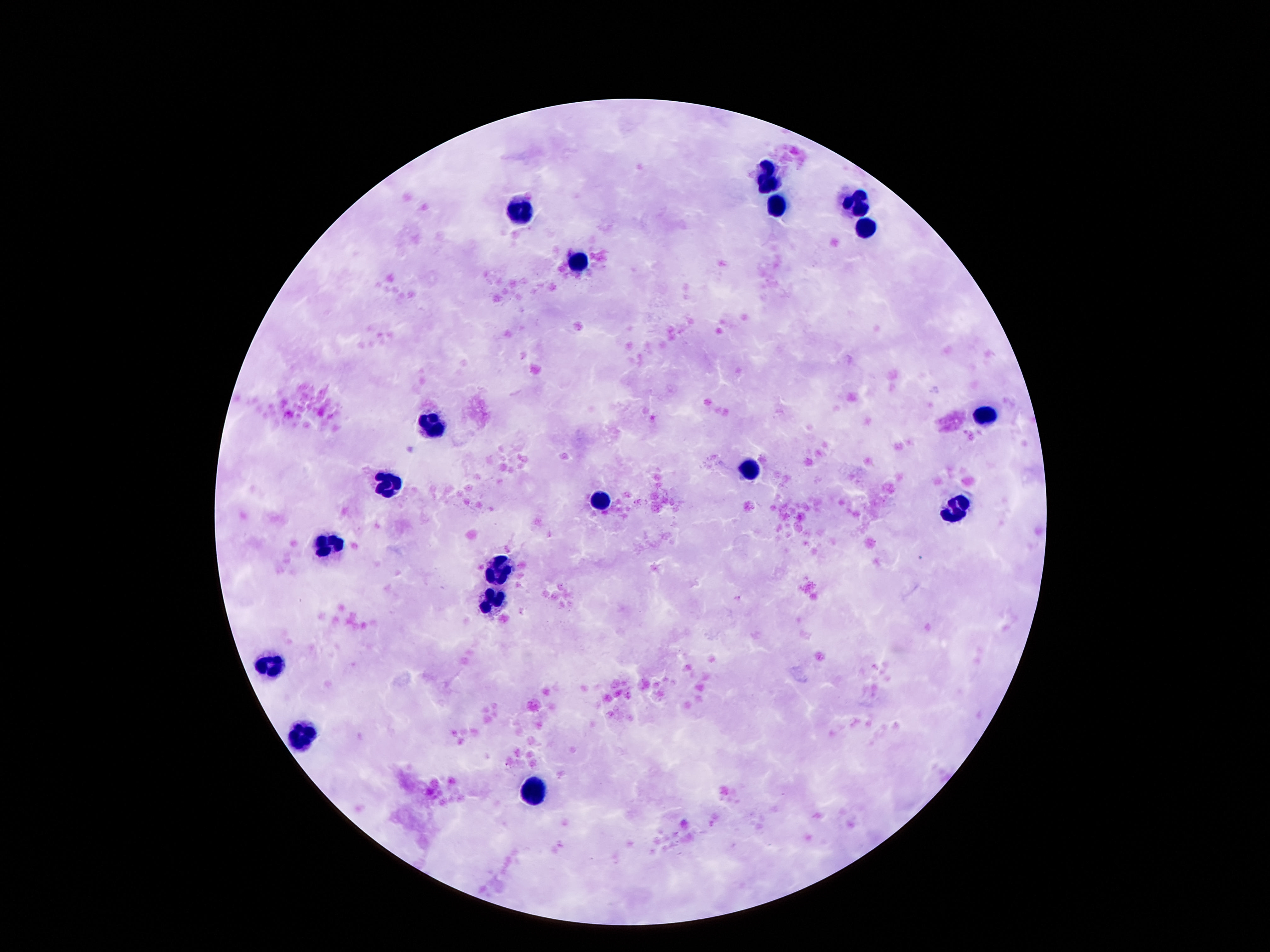

capture: smartphone camera through the microscope eyepiece
magnification: 100x
patient_malaria_status: negative
stain: Giemsa
leukocyte_locations: 'approximate centers as {x, y} in pixels: {767, 180}, {778, 205}, {857, 206}, {517, 209}, {866, 233}, {579, 260}, {984, 416}, {431, 421}, {751, 470}, {389, 486}, {599, 500}, {959, 510}, {329, 545}, {502, 570}, {495, 604}, {272, 666}, {309, 731}, {533, 786}'
field_of_view: single
image_size: 1270×952 pixels
preparation: thick peripheral-blood smear